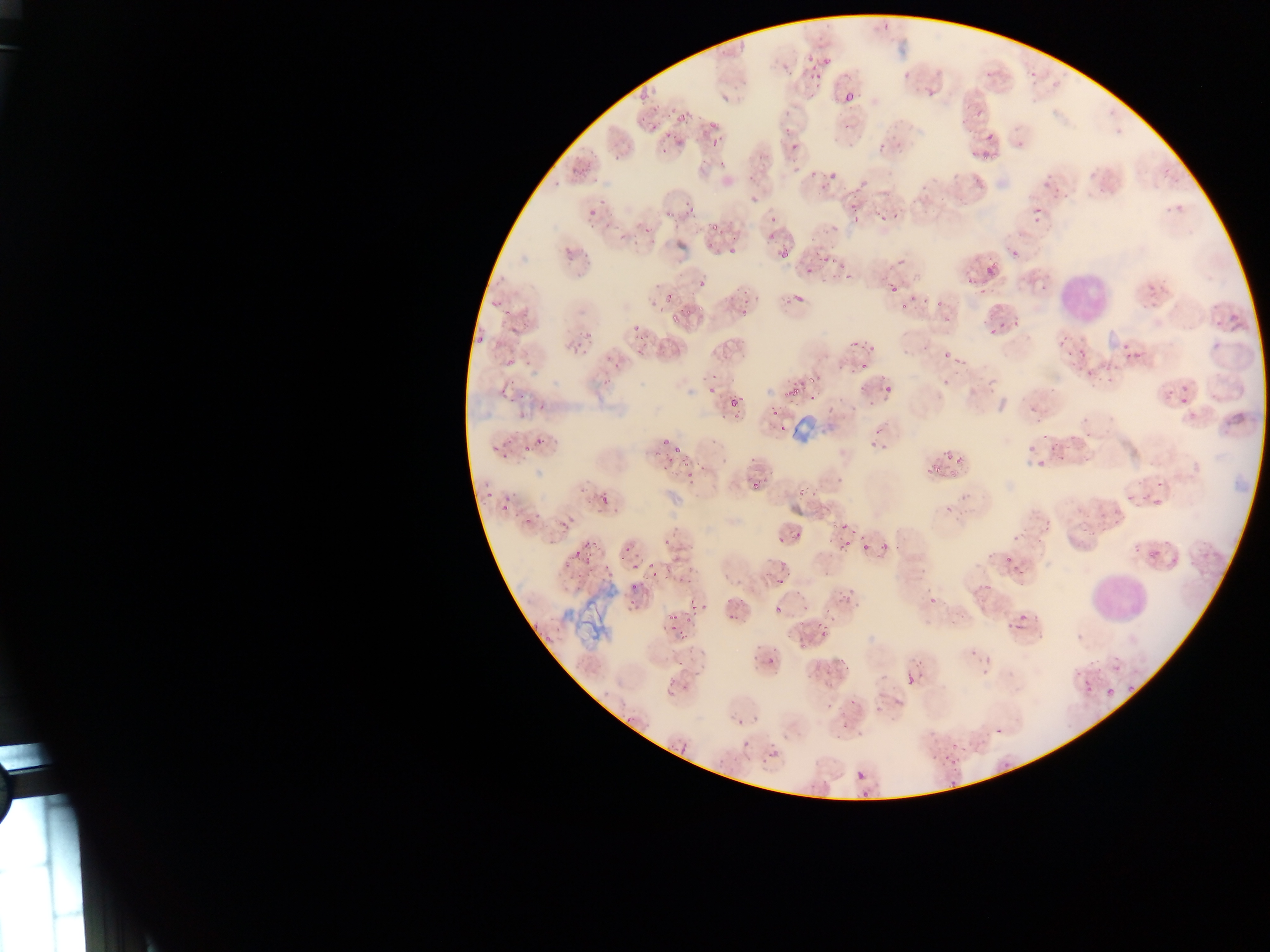

Approximate bounding boxes as (left, top, right, bottom) in pixels.
Summary:
  - Artifact (stain precipitate or debris) locations (subset; some below the resolvable size): (891, 44, 911, 60), (793, 415, 819, 440), (573, 588, 621, 644)
  - Leukocyte locations: (1058, 271, 1111, 323), (1092, 573, 1146, 618)
  - Plasmodium parasite locations (subset; some below the resolvable size): (804, 56, 813, 61), (810, 64, 817, 72), (903, 72, 908, 80), (845, 93, 854, 101), (721, 96, 730, 101), (679, 115, 684, 124), (708, 121, 716, 129), (711, 139, 720, 145), (878, 141, 884, 151), (614, 152, 622, 160), (990, 152, 999, 162), (982, 154, 988, 162), (749, 192, 760, 205), (849, 199, 856, 209), (599, 200, 607, 204), (684, 202, 692, 206), (1034, 208, 1042, 213), (589, 210, 597, 216), (852, 216, 857, 224), (714, 223, 717, 231), (645, 228, 653, 233), (620, 235, 628, 240), (583, 247, 589, 259), (780, 248, 788, 259), (822, 254, 829, 262), (987, 266, 994, 275), (804, 267, 813, 273), (575, 273, 583, 277), (845, 274, 854, 279), (699, 279, 706, 287), (889, 285, 895, 293), (978, 290, 986, 294), (795, 291, 805, 302), (490, 302, 498, 308), (660, 306, 663, 314), (477, 335, 482, 343), (944, 352, 952, 358), (1135, 352, 1142, 360), (1127, 353, 1136, 357), (505, 358, 515, 367), (601, 379, 609, 385), (707, 388, 717, 394), (1181, 398, 1189, 403), (731, 400, 739, 407), (540, 401, 543, 411), (537, 437, 542, 445), (663, 438, 670, 446), (676, 446, 680, 454), (687, 473, 695, 478), (1143, 492, 1148, 500), (604, 493, 607, 505), (535, 512, 540, 520), (561, 521, 569, 529), (562, 528, 571, 532), (862, 543, 868, 551), (573, 552, 581, 557), (825, 568, 831, 576), (775, 579, 784, 584), (671, 612, 676, 622), (729, 612, 738, 621), (820, 629, 826, 639), (543, 634, 552, 642), (1128, 686, 1136, 694), (825, 700, 833, 710), (849, 700, 858, 706), (739, 718, 743, 726), (995, 727, 1000, 735), (743, 740, 748, 748), (857, 769, 863, 778), (949, 780, 957, 785), (862, 788, 867, 797) | approximate (x, y) pixel centers of objects too small to bound: (886, 27), (784, 67), (818, 76), (654, 109), (673, 111), (787, 112), (668, 115), (643, 120), (653, 128), (787, 130), (668, 136), (793, 147), (664, 150), (795, 170), (813, 174), (833, 175), (557, 184), (1178, 208), (1168, 210), (690, 211), (667, 215), (883, 219), (774, 220), (1036, 220), (592, 226), (607, 226), (771, 236), (731, 251), (1015, 253), (570, 259), (658, 285), (668, 297), (939, 304), (903, 308), (674, 317), (1219, 321), (1001, 324), (1016, 325), (635, 328), (991, 332), (579, 333), (855, 344), (579, 345), (1125, 346), (1217, 346), (585, 351), (616, 363), (865, 367), (1090, 374), (715, 377), (1110, 379), (810, 380), (796, 389), (1184, 389), (502, 391), (889, 391), (793, 394), (784, 395), (523, 396), (813, 398), (512, 401), (776, 414), (1086, 434), (1068, 446), (495, 447), (1052, 448), (528, 449), (950, 457), (1061, 459), (1086, 459), (953, 473), (1159, 483), (489, 494), (1130, 497), (506, 498), (590, 502), (504, 509), (599, 510), (614, 512), (515, 515), (529, 521), (1047, 522), (843, 526), (853, 533), (798, 535), (781, 540), (667, 542), (847, 542), (841, 546), (885, 546), (626, 549), (1151, 555), (621, 557), (588, 559), (1008, 559), (650, 565), (634, 567), (653, 574), (634, 587), (631, 602), (637, 607), (703, 607), (693, 608), (777, 610), (674, 627), (682, 637), (769, 662), (628, 721), (771, 745), (1004, 765)
  - Image size: 1270×952 pixels
  - Country: Ghana
  - Preparation: thin blood film
  - Field of view: single
  - Capture: mobile-phone photograph through a microscope